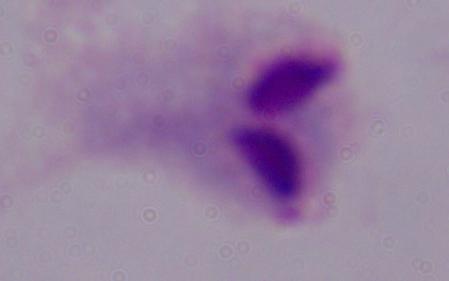
Summary:
  - Modality: photomicrograph
  - Identification: trichomonad
  - Magnification: 1000x